Point out each leukocyte.
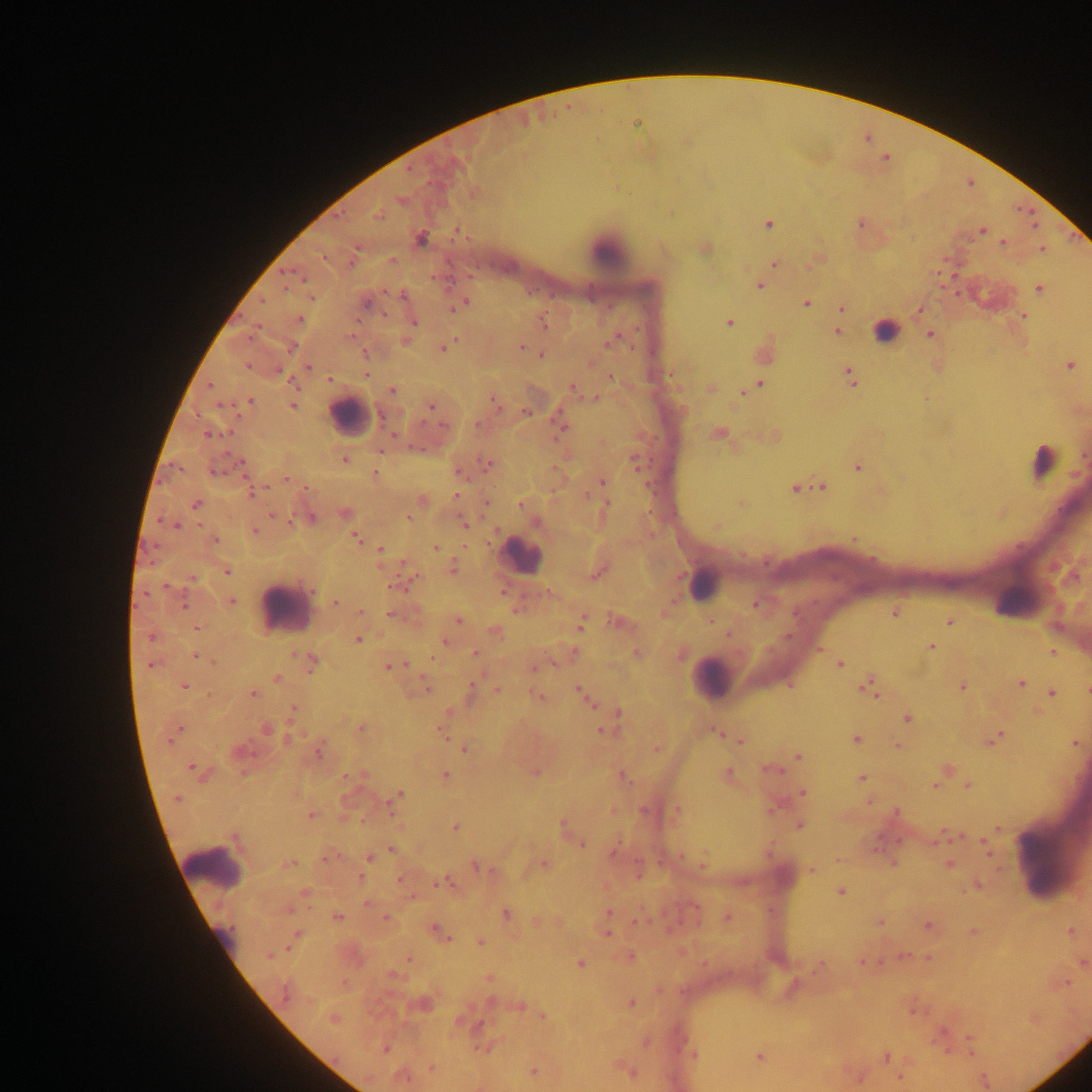

Approximate centers as x y in pixels.
Leukocytes: 607 251; 350 416; 522 555; 702 583; 285 607; 710 678; 215 869.

Plasmodium parasite locations: 637 123; 861 223; 768 224; 1035 224; 981 230; 457 232; 421 238; 1003 243; 1042 249; 392 259; 774 263; 759 286; 1039 289; 402 295; 312 298; 262 301; 462 303; 807 303; 366 304; 842 307; 920 310; 1023 316; 300 319; 413 321; 729 322; 544 324; 836 331; 886 331; 929 335; 405 341; 609 343; 292 347; 521 347; 444 348; 541 355; 1070 366; 307 367; 367 374; 610 376; 850 376; 330 379; 760 384; 210 386; 573 388; 392 390; 744 392; 595 398; 250 401; 496 403; 431 405; 293 406; 526 413; 442 425; 478 425; 560 428; 212 434; 719 434; 344 459; 634 460; 242 463; 488 465; 857 467; 215 470; 459 472; 375 473; 286 479; 602 482; 822 486; 795 488; 251 492; 457 497; 521 504; 607 504; 196 505; 345 512; 273 516; 408 517; 312 518; 177 525; 465 525; 717 527; 254 532; 355 538; 854 539; 216 540; 435 547; 381 550; 453 569; 226 572; 596 574; 191 579; 414 579; 166 585; 394 586; 502 593; 232 601; 335 602; 755 604; 184 606; 360 611; 390 614; 895 614; 612 619; 458 620; 711 621; 950 621; 580 626; 197 628; 494 632; 727 634; 150 637; 357 640; 445 642; 930 646; 820 650; 1053 652; 475 653; 294 655; 196 656; 433 658; 312 662; 840 664; 150 665; 389 667; 534 668; 277 678; 1021 684; 184 686; 426 687; 962 687; 870 688; 497 689; 471 691; 1087 691; 580 692; 1052 693; 252 694; 538 697; 588 701; 293 709; 619 715; 907 718; 266 729; 361 729; 178 730; 443 732; 602 732; 718 733; 172 736; 856 738; 289 739; 996 739; 740 740; 1075 744; 897 745; 465 749; 657 750; 318 752; 798 756; 193 768; 773 771; 727 772; 349 776; 445 776; 622 777; 861 778; 968 785; 935 786; 803 793; 399 794; 177 798; 392 805; 773 810; 644 811; 677 811; 896 812; 311 815; 564 825; 799 825; 455 827; 957 836; 582 844; 985 846; 392 849; 614 851; 326 858; 370 858; 703 863; 893 863; 289 864; 950 864; 544 865; 477 866; 811 870; 360 877; 400 879; 442 883; 978 886; 841 891; 305 893; 367 904; 695 906; 609 913; 507 915; 338 917; 386 918; 727 918; 639 920; 881 922; 927 925; 436 930; 974 931; 1070 931; 608 934; 296 935; 481 942; 268 956; 631 956; 905 956; 929 958; 409 960; 1083 961; 580 963; 862 963; 821 964; 393 975; 489 978; 1067 983; 285 994; 630 1003; 520 1005; 543 1016; 333 1019; 970 1039; 482 1048; 385 1050; 694 1055; 760 1057; 886 1058; 432 1067; 628 1071; 533 1072; 901 1078; 404 1079; 985 1081. Image is 1092×1092 pixels. Thick blood film. One field of view. Collected in Ghana. Mobile-phone photograph taken through the microscope.